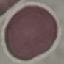
Summary:
  - Malaria status: uninfected
  - Preparation: thin blood film
  - Capture: smartphone through the microscope eyepiece
  - Stain: Giemsa
  - Image type: cell patch, automatically extracted from a larger field of view and resized to 64 × 64 pixels